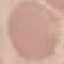 Result: no malaria parasites detected. Acquired by smartphone through the microscope eyepiece. Thin smear of blood. Automatically extracted cell patch, resized to 64 × 64 pixels. Giemsa stain.